Give a bounding box for every leukocyte visible.
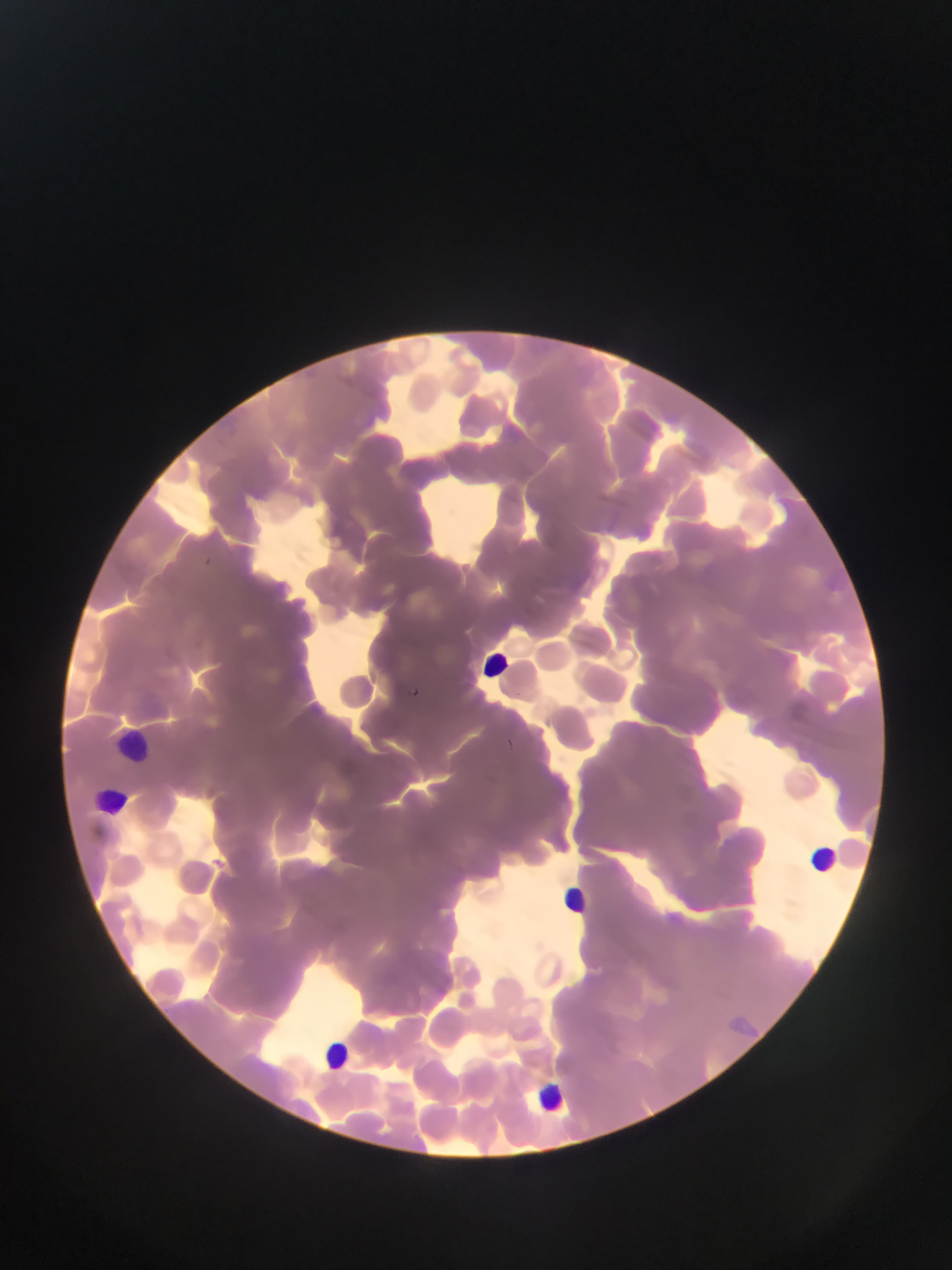
Approximate bounding boxes as left top right bottom in pixels.
Leukocytes: 480 644 515 682; 117 734 152 762; 98 787 128 811; 814 841 833 871; 560 881 603 928; 327 1038 349 1068; 534 1084 566 1112.

Summary:
  - Malaria parasite locations: 203 554 215 571; 408 685 427 697; 508 737 516 749
  - Country: Ghana
  - Image size: 952×1270 pixels
  - Field of view: single
  - Preparation: thin blood film
  - Capture: mobile-phone photograph through a microscope